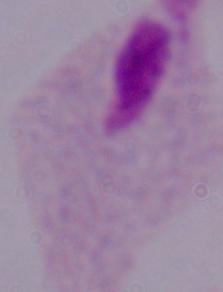

identification = trichomonad
magnification = 1000x
modality = photomicrograph